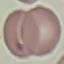
Malaria status: uninfected. Thin smear of blood. Giemsa stain. Acquired by smartphone through the microscope eyepiece. Automatically extracted cell patch, resized to 64 × 64 pixels.